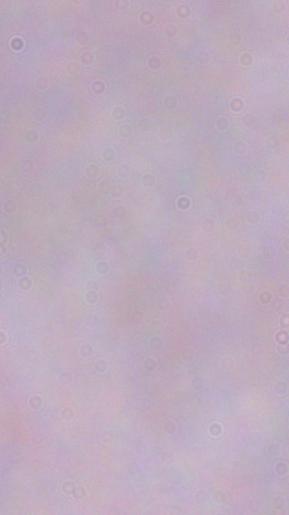
Summary:
  - Magnification: 1000x
  - Identification: trypanosome
  - Modality: photomicrograph